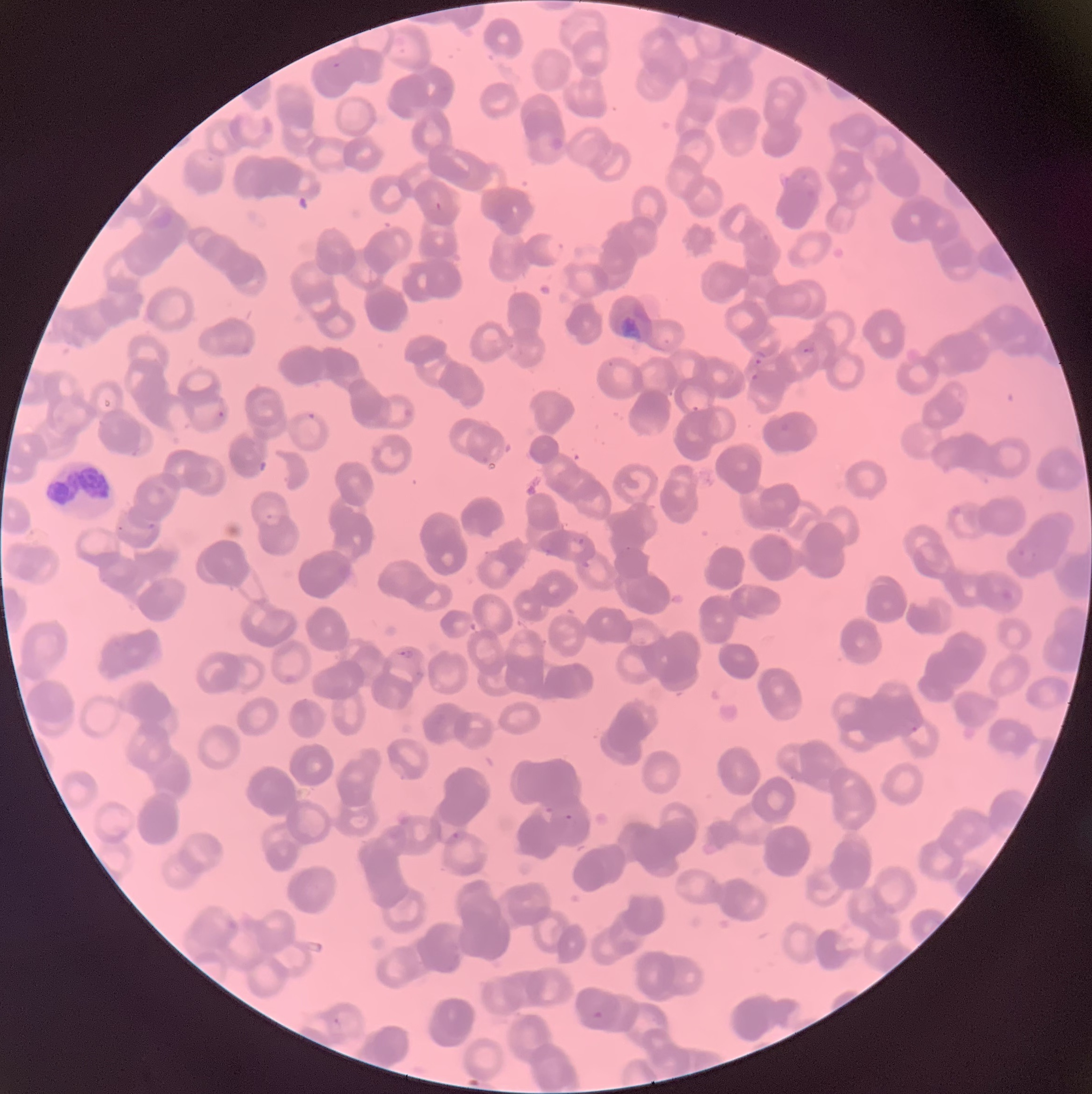 Approximate bounding boxes as [x1, y1, x2, y2] in pixels. Plasmodium parasite locations: [435, 202, 442, 211], [802, 347, 814, 354], [753, 358, 762, 364], [750, 373, 758, 381], [691, 406, 699, 412], [306, 412, 317, 422], [147, 523, 155, 530], [578, 537, 585, 546], [398, 649, 415, 660], [564, 814, 573, 821], [451, 831, 460, 841], [592, 1010, 605, 1021]. Plasmodium parasites too small for a box (approximate centers as [x, y] in pixels): [336, 65], [220, 414], [914, 729]. White blood cell locations: [45, 460, 115, 516]. The red blood cells show rouleaux formation. Light microscopy. Image is 1092×1094 pixels. Thin blood film.